Describe the morphology of the erythrocytes.
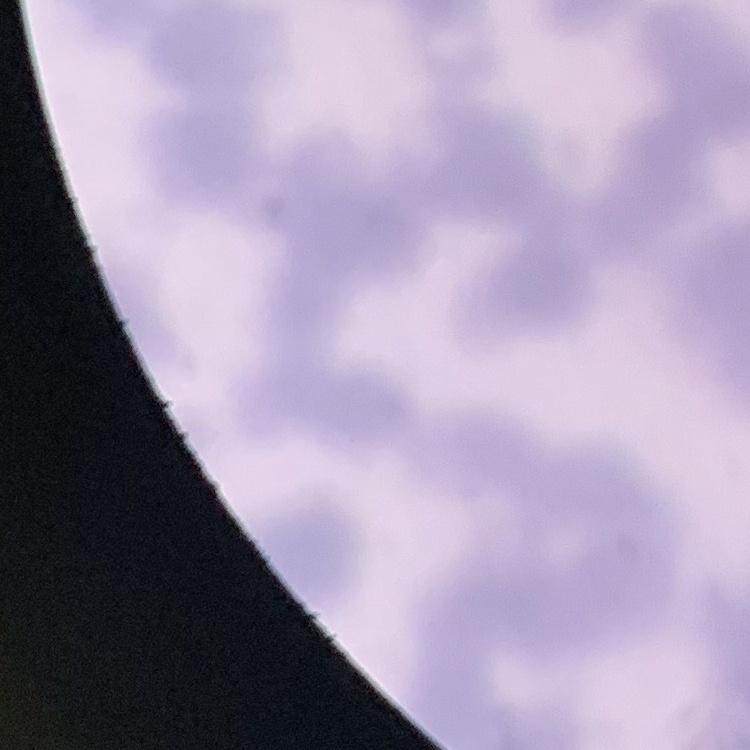
They show rouleaux formation.

stain: Field's or Giemsa
preparation: thin blood film
image_type: one tile cut from a larger photomicrograph